Classify this cell by malaria status.
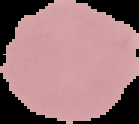
It is uninfected.

Summary:
  - Preparation: thin blood film
  - Image type: segmented cell region on a black background
  - Image size: 139×124 pixels